Locate and identify every blood parasite.
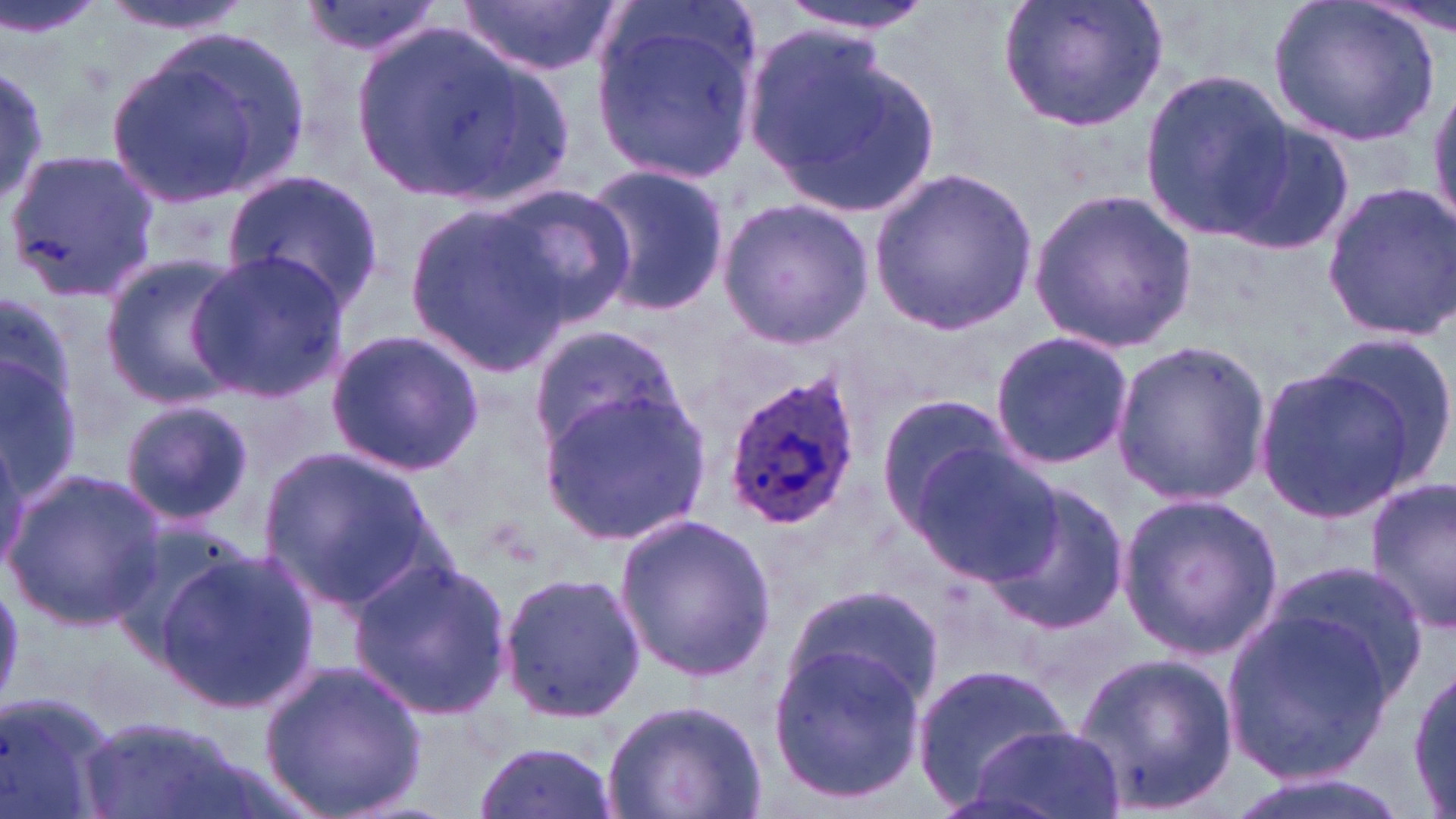

Approximate bounding boxes as (x1, y1, x2, y2) in pixels.
Plasmodium ovale-infected red blood cells: (721, 365, 866, 532).
No Plasmodium falciparum, Plasmodium malariae, Plasmodium vivax, Babesia divergens, or Trypanosoma brucei observed.

Summary:
  - Uninfected red blood cell locations: (0, 0, 109, 42), (97, 0, 253, 35), (295, 0, 450, 59), (457, 0, 622, 77), (777, 0, 939, 35), (998, 0, 1168, 133), (1270, 0, 1442, 148), (589, 3, 761, 186), (348, 23, 536, 202), (742, 24, 937, 215), (103, 30, 310, 209), (1139, 69, 1293, 241), (1425, 81, 1456, 232), (1222, 118, 1356, 255), (4, 146, 161, 302), (579, 162, 731, 318), (870, 167, 1038, 334), (222, 170, 382, 311), (1318, 180, 1456, 343), (490, 184, 637, 325), (1027, 187, 1196, 354), (715, 198, 875, 348), (405, 205, 569, 371), (185, 251, 348, 399), (98, 253, 251, 406), (0, 297, 84, 503), (527, 323, 688, 458), (325, 330, 484, 474), (1315, 331, 1456, 482), (989, 332, 1136, 469), (1109, 342, 1272, 506), (1250, 364, 1425, 522), (539, 390, 709, 543), (875, 393, 1019, 524), (119, 400, 255, 528), (906, 444, 1062, 586), (258, 448, 435, 611), (2, 469, 166, 628), (1364, 477, 1456, 636), (983, 482, 1133, 636), (1115, 493, 1283, 660), (615, 513, 777, 681), (156, 545, 317, 712), (349, 554, 514, 720), (493, 568, 646, 724), (786, 582, 946, 711), (1220, 607, 1401, 782), (767, 644, 926, 802), (1073, 652, 1239, 814), (259, 657, 426, 819), (911, 662, 1074, 803), (1409, 663, 1455, 813), (0, 689, 119, 819), (601, 697, 769, 819), (78, 713, 256, 819), (963, 724, 1122, 819), (470, 741, 621, 819), (1214, 769, 1415, 819)
  - Slide-level diagnosis: Plasmodium ovale
  - Stain: May-Grünwald-Giemsa
  - Magnification: 1000x
  - Field of view: single
  - Image size: 1456×819 pixels
  - Modality: light microscopy
  - Preparation: thin blood film